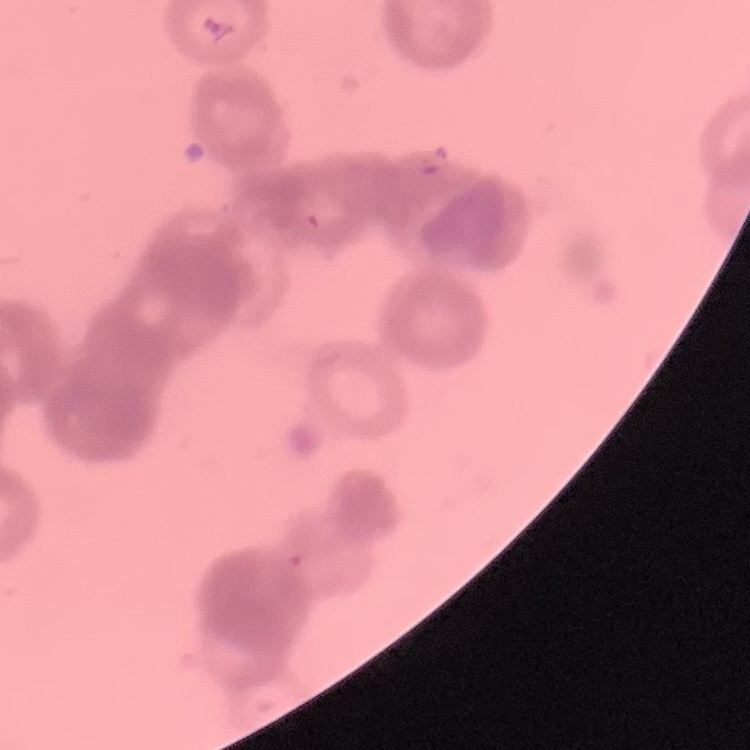
Summary:
  - Red blood cell morphology: rouleaux formation
  - Preparation: thin blood film
  - Image type: square crop of a larger photomicrograph
  - Stain: Field's or Giemsa